Point out every Plasmodium parasite.
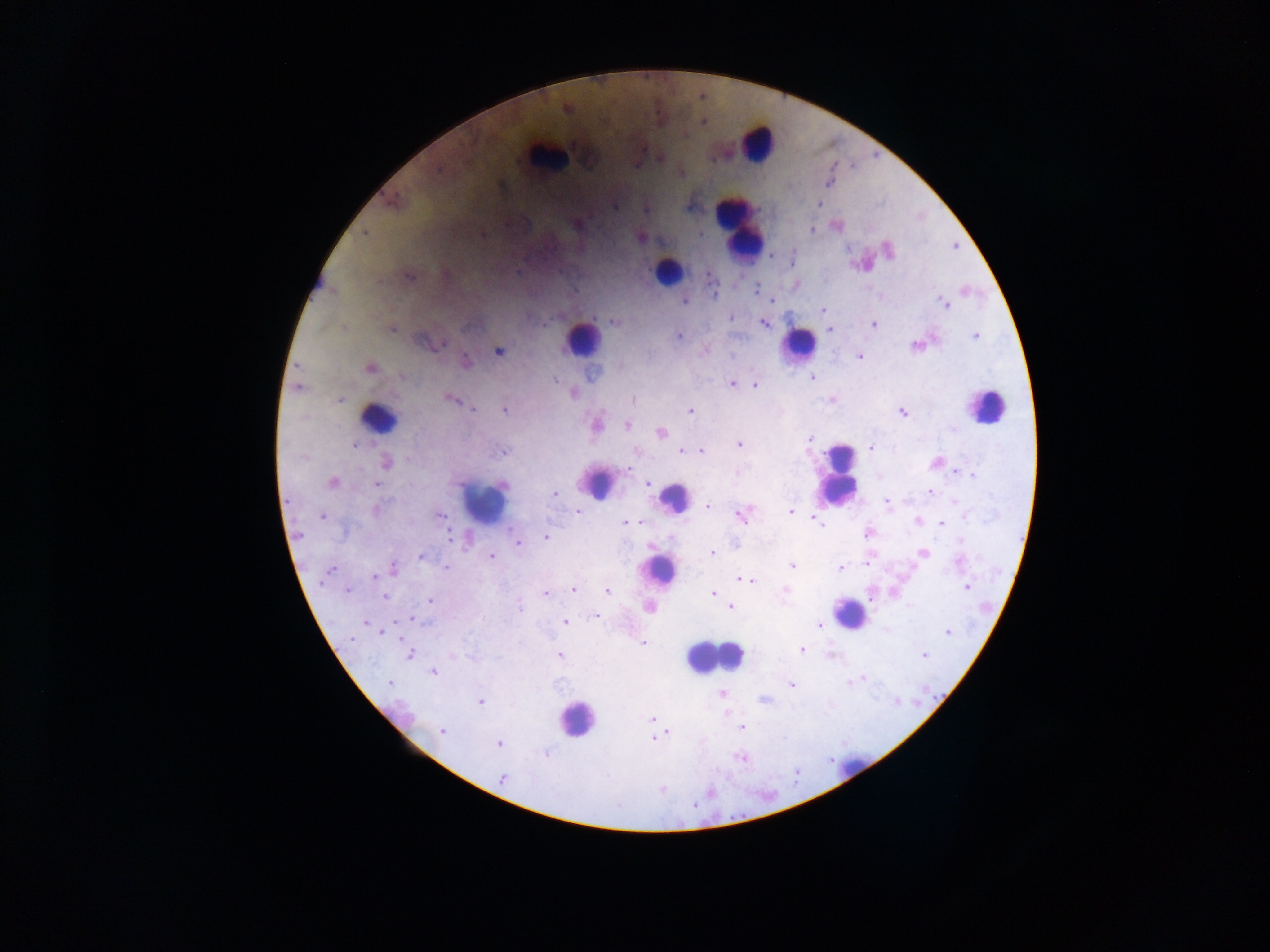
Approximate centers as (x, y) in pixels.
Plasmodium parasites: (438, 170), (828, 184), (502, 186), (820, 204), (614, 206), (688, 208), (645, 210), (576, 224), (811, 229), (365, 233), (639, 238), (955, 247), (889, 250), (518, 271), (411, 277), (757, 289), (684, 302), (945, 304), (822, 310), (731, 319), (614, 322), (764, 323), (874, 325), (344, 328), (392, 330), (830, 330), (678, 335), (975, 336), (426, 342), (442, 345), (916, 346), (498, 351), (705, 351), (859, 356), (465, 362), (370, 368), (401, 376), (813, 378), (555, 380), (732, 383), (755, 385), (297, 388), (574, 394), (450, 399), (633, 399), (339, 400), (474, 409), (504, 410), (690, 411), (903, 414), (597, 425), (626, 426), (953, 429), (661, 432), (810, 440), (739, 444), (354, 445), (871, 448), (682, 451), (688, 451), (701, 451), (503, 452), (385, 463), (627, 470), (956, 472), (973, 475), (333, 482), (648, 484), (376, 485), (502, 485), (930, 492), (554, 493), (955, 501), (887, 502), (708, 506), (376, 510), (577, 511), (790, 511), (441, 515), (741, 516), (965, 516), (322, 517), (917, 521), (626, 522), (817, 522), (941, 523), (867, 532), (450, 537), (545, 538), (961, 542), (518, 544), (712, 553), (922, 553), (491, 556), (421, 557), (868, 562), (959, 562), (793, 566), (393, 568), (446, 568), (839, 569), (329, 570), (374, 577), (741, 578), (747, 580), (967, 587), (573, 589), (785, 589), (347, 590), (608, 591), (545, 593), (712, 593), (385, 596), (430, 601), (519, 607), (731, 607), (649, 609), (596, 617), (411, 619), (565, 622), (366, 623), (820, 624), (947, 633), (352, 639), (643, 643), (802, 649), (408, 654), (559, 655), (924, 655), (434, 672), (861, 678), (389, 682), (849, 683), (791, 684), (721, 693), (763, 701), (481, 702), (652, 719), (742, 728), (442, 731), (667, 732), (653, 739), (498, 743), (546, 754), (740, 758), (502, 778), (662, 790), (710, 791), (694, 805).

Leukocyte locations: (757, 142), (545, 156), (738, 228), (669, 269), (583, 338), (799, 343), (987, 406), (378, 419), (839, 473), (600, 484), (674, 497), (484, 503), (657, 567), (848, 615), (712, 657), (399, 715), (577, 717), (849, 767). Image is 1270×952 pixels. Photographed through a microscope with a mobile-phone camera. Single field of view. Collected in Ghana. Thick blood smear.